State the preparation type.
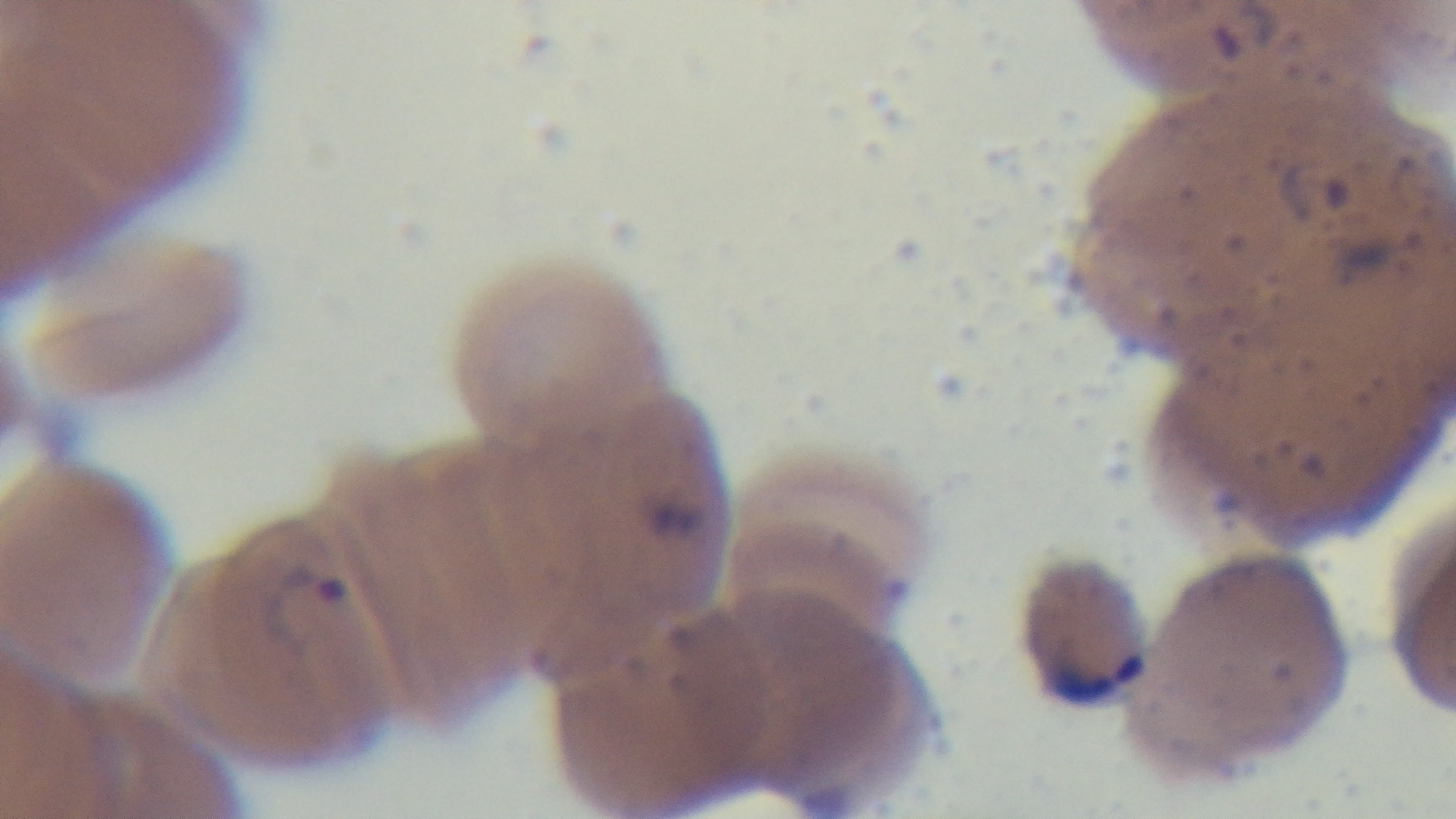
A thin smear.

Summary:
  - Objective: 100x oil immersion
  - Capture: mounted 4K digital camera
  - Modality: light microscopy
  - Field of view: one from the slide
  - Stain: Giemsa
  - Malaria status: positive